Assess this cell for malaria.
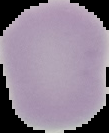

It is uninfected.

Summary:
  - Image size: 109×133 pixels
  - Preparation: thin blood smear
  - Image type: segmented cell region on a black background